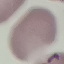

Summary:
  - Malaria status: uninfected
  - Preparation: thin blood film
  - Stain: Giemsa
  - Image type: automatically extracted cell patch, resized to 64 × 64 pixels
  - Capture: smartphone through the microscope eyepiece